Report the malaria status of this cell.
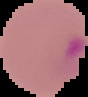

Parasitized.

Cell region segmented out of the field of view; the surrounding area is masked to black. From a thin blood film. Image is 88×97 pixels.